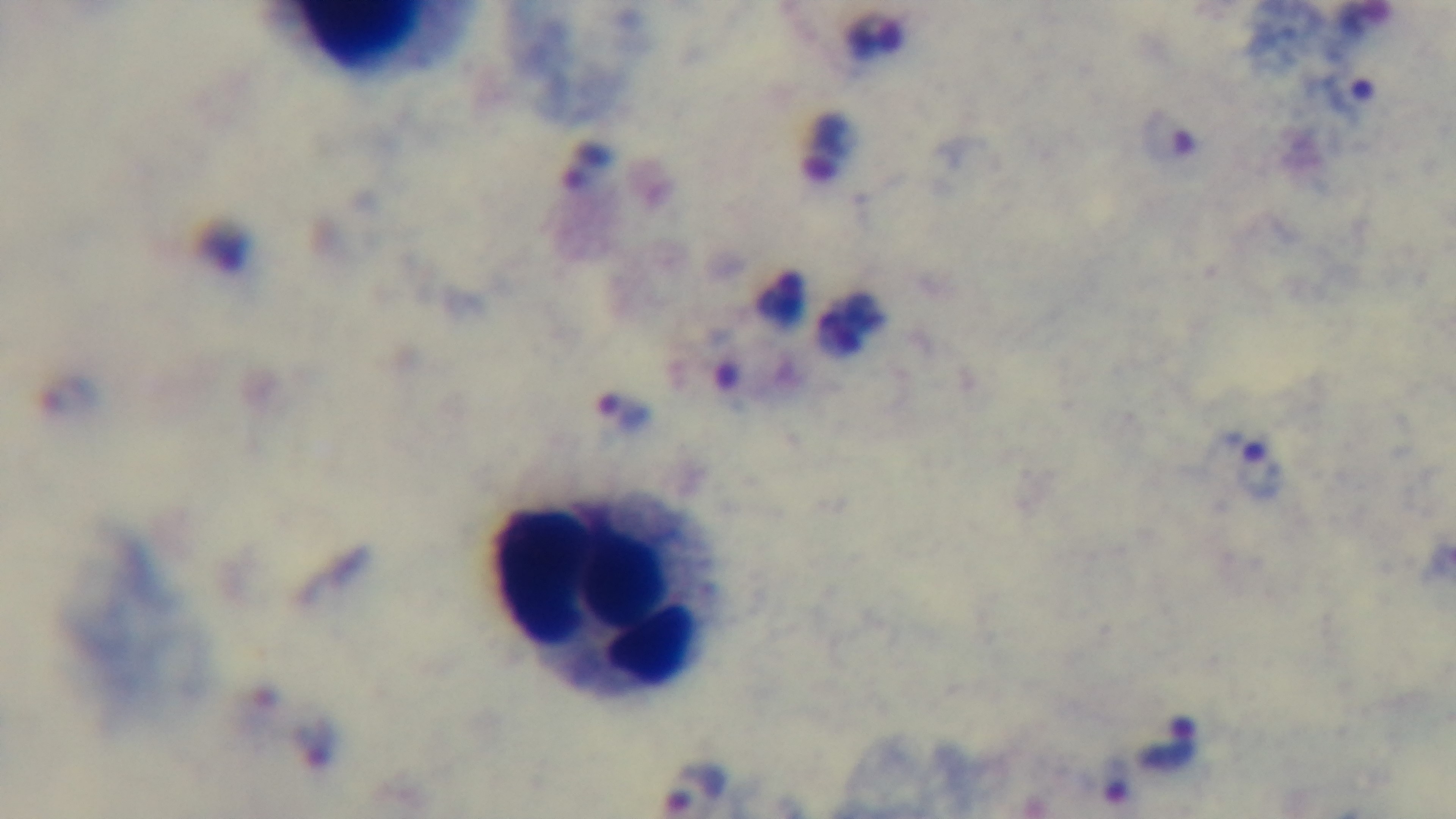

stain = Giemsa
objective = 100x oil immersion
modality = light microscopy
capture = mounted 4K digital camera
malaria status = infected
field of view = single
preparation = thick smear